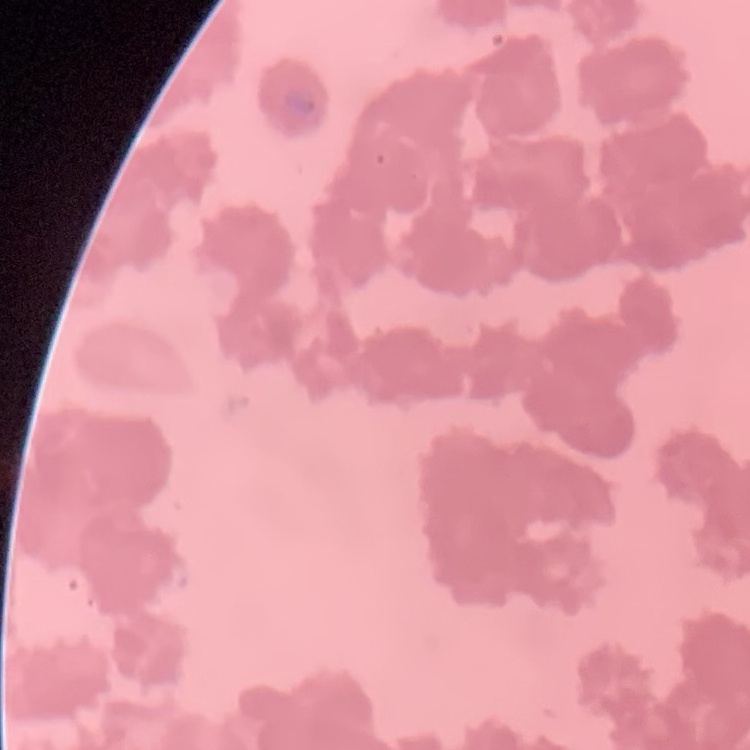 The erythrocytes exhibit rouleaux formation. Stained with either Field's or Giemsa. Square crop of a larger photomicrograph. Thin blood film.